Point out each Plasmodium parasite.
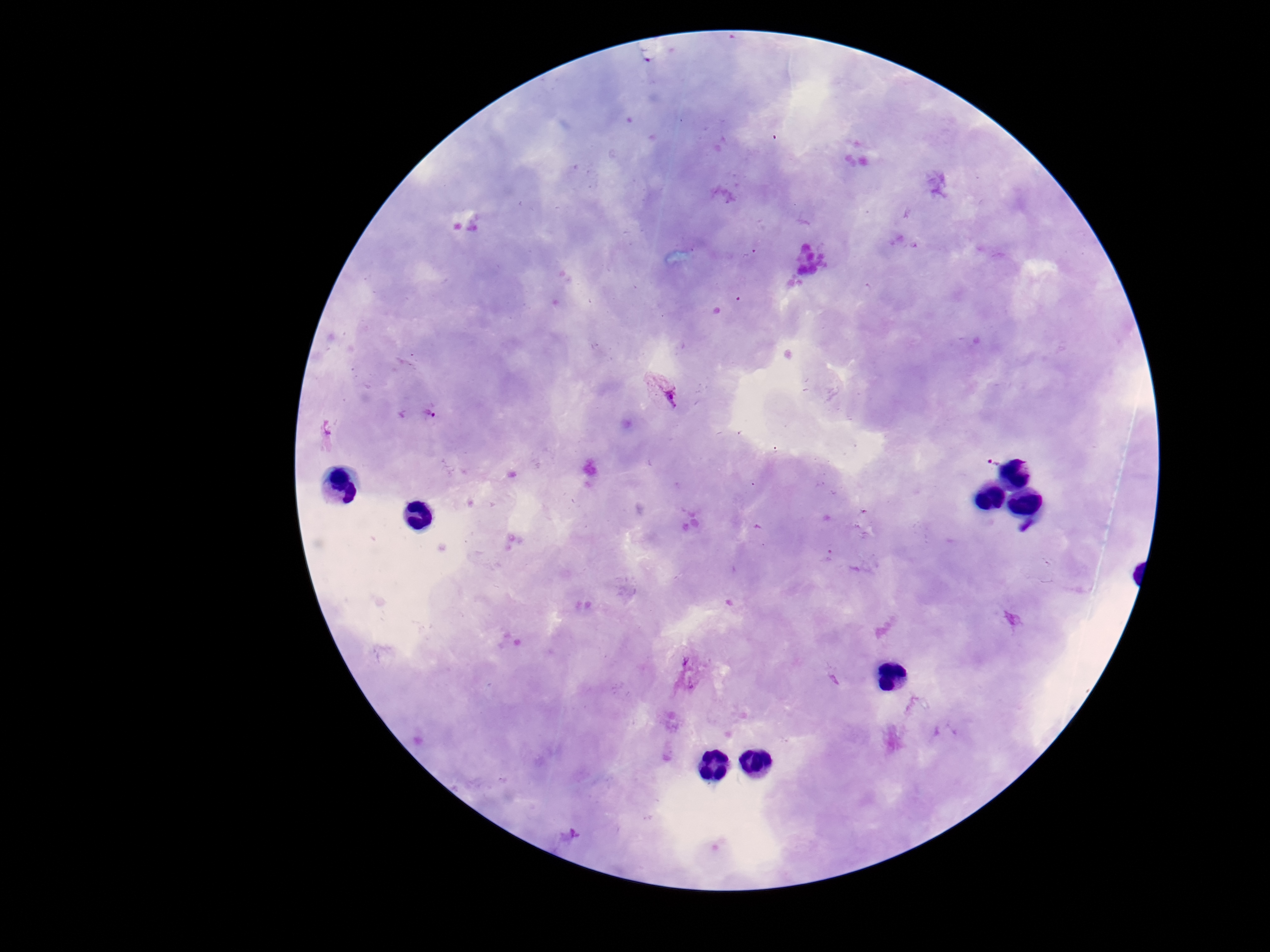

Approximate centers as {x, y} in pixels.
Plasmodium parasites: {661, 389}, {415, 414}, {992, 461}.

{
  "preparation": "thick blood smear",
  "stain": "Giemsa",
  "capture": "smartphone camera through the microscope eyepiece",
  "patient_malaria_status": "infected",
  "magnification": "100x",
  "image_size": "1270×952 pixels",
  "field_of_view": "one from this slide"
}